Point out each malaria parasite.
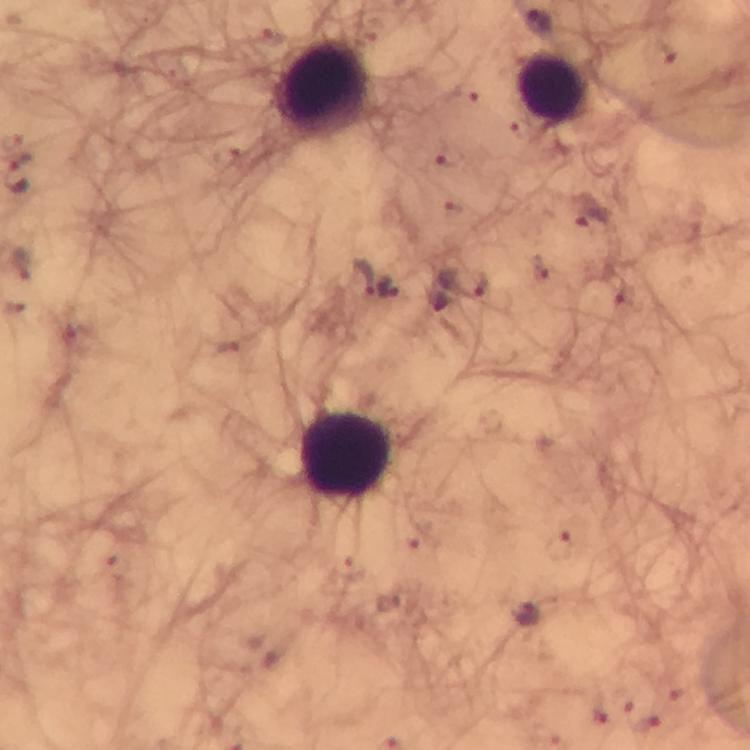
Approximate centers as [x, y] in pixels.
Malaria parasites: [539, 22], [589, 219], [361, 278], [465, 282], [525, 613], [641, 714].

Summary:
  - Leukocyte locations: [320, 86], [554, 88], [345, 455]
  - Stain: Giemsa
  - Cropped from: one field of view
  - Preparation: thick blood smear
  - Image size: 750×750 pixels
  - Capture: smartphone photograph through a microscope
  - Immersion oil: used
  - Magnification: 100x
  - Context: from a malaria diagnostic workup